Classify this cell by malaria status.
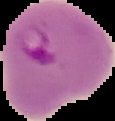

It is parasitized.

Summary:
  - Preparation: thin blood smear
  - Image type: segmented cell region with the area outside set to black
  - Image size: 115×121 pixels